Classify this cell by malaria status.
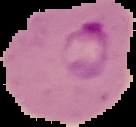
Parasitized.

Summary:
  - Preparation: thin blood film
  - Image size: 136×127 pixels
  - Image type: segmented cell region on a black background